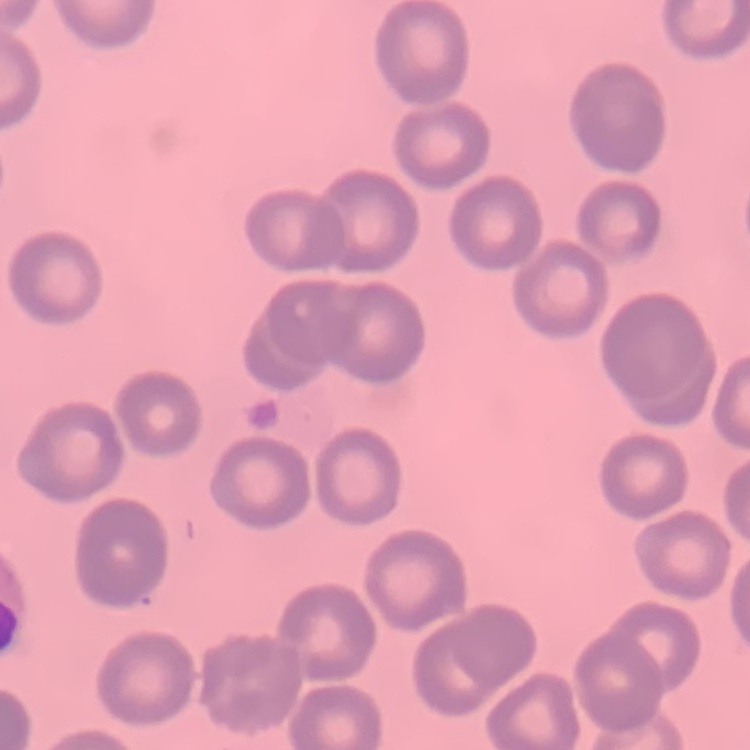

erythrocyte_morphology: no rouleaux formation
stain: Field's or Giemsa
preparation: thin blood film
image_type: square crop of a larger photomicrograph